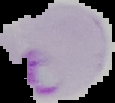
Image is 115×103 pixels. Result: Plasmodium parasites detected. From a thin blood smear. Cell region segmented out of the field of view; the surrounding area is masked to black.